Assess this cell for malaria.
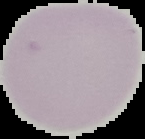

Uninfected.

Image is 145×139 pixels. Cell region segmented out of the field of view; the surrounding area is masked to black. From a thin blood smear.